Assess this cell for malaria.
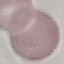
It is uninfected.

Automatically extracted cell patch, resized to 64 × 64 pixels. Thin blood smear. Acquired by smartphone through the microscope eyepiece. Giemsa stain.